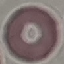
Result: no malaria parasites seen. Giemsa stain. Photographed with a smartphone camera at the microscope eyepiece. Thin smear of blood. Cell patch, automatically extracted from a larger field of view and resized to 64 × 64 pixels.